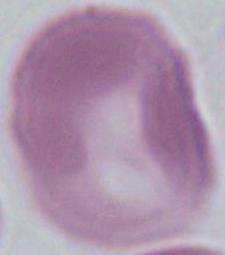
Summary:
  - Identification: red blood cell
  - Modality: micrograph
  - Magnification: 1000x